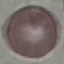

malaria status = uninfected
stain = Giemsa
capture = smartphone through the microscope eyepiece
image type = cell patch, automatically extracted from a larger field of view and resized to 64 × 64 pixels
preparation = thin smear